Describe the morphology of the red blood cells.
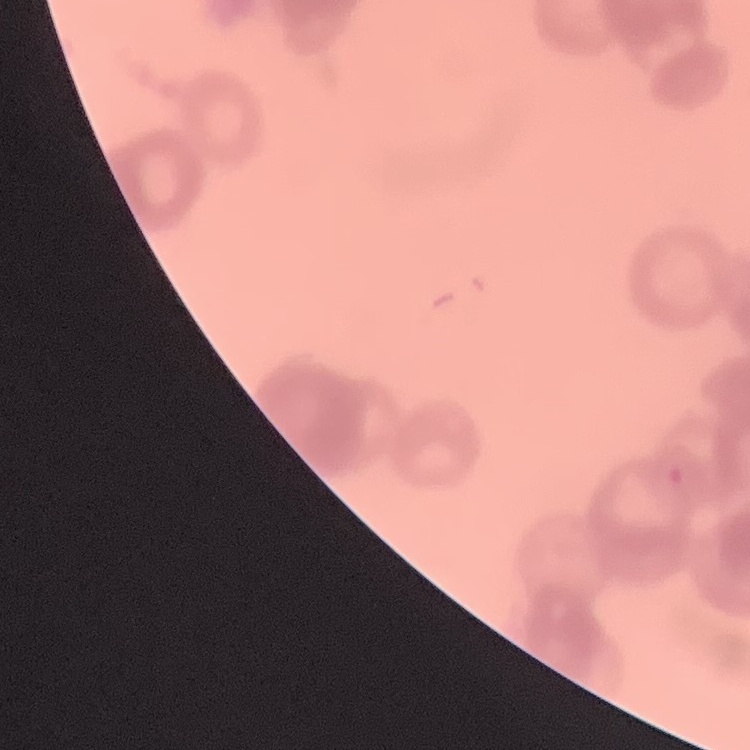

Rouleaux formation.

Stained with either Field's or Giemsa. Thin blood film. Square crop of a larger photomicrograph.